Describe the morphology of the erythrocytes.
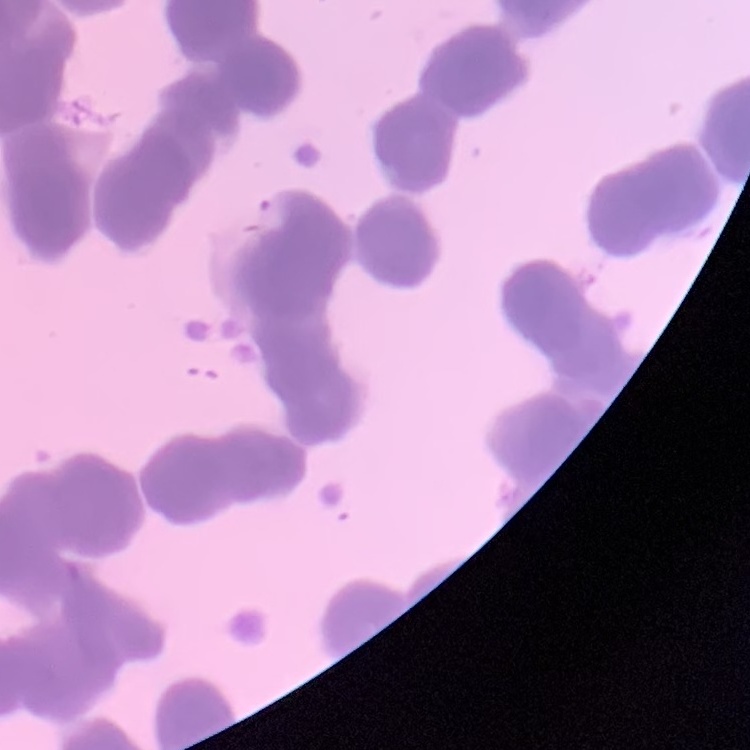

They show rouleaux formation.

Thin blood smear. One tile cut from a larger photomicrograph. Field's or Giemsa stain.